Locate and identify every blood parasite.
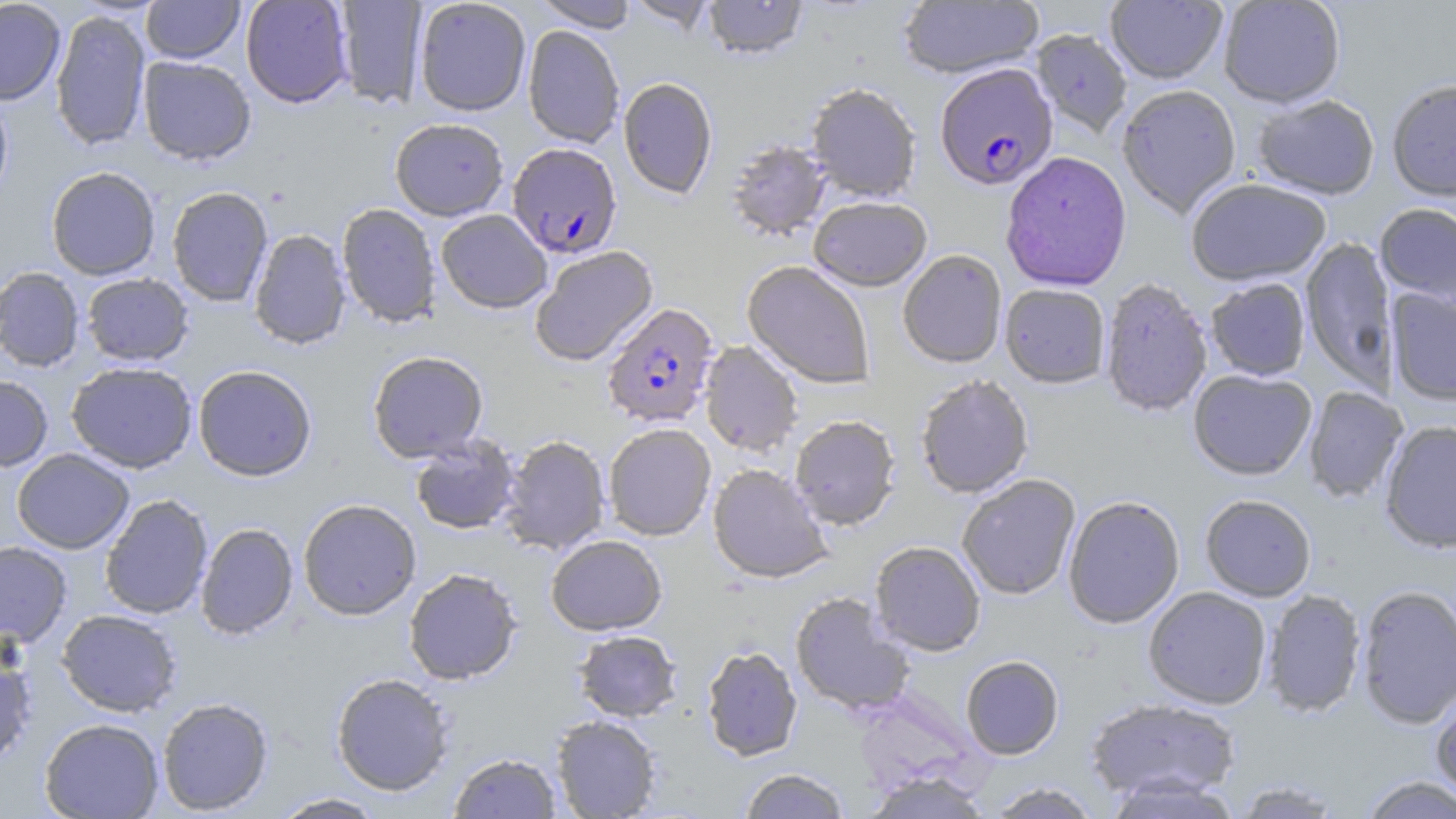

Approximate bounding boxes as named x1/y1/x2/y2 corners in pixels.
Plasmodium falciparum-infected red blood cells: (x1=934, y1=63, x2=1057, y2=190), (x1=507, y1=142, x2=622, y2=258), (x1=602, y1=303, x2=719, y2=429).
No Plasmodium ovale, Plasmodium malariae, Plasmodium vivax, Babesia divergens, or Trypanosoma brucei observed.

Summary:
  - Uninfected red blood cell locations: (x1=0, y1=0, x2=66, y2=105), (x1=141, y1=0, x2=244, y2=64), (x1=240, y1=0, x2=354, y2=108), (x1=413, y1=0, x2=531, y2=116), (x1=533, y1=0, x2=639, y2=32), (x1=624, y1=0, x2=718, y2=33), (x1=703, y1=0, x2=807, y2=60), (x1=1106, y1=0, x2=1226, y2=85), (x1=1218, y1=0, x2=1345, y2=108), (x1=333, y1=1, x2=428, y2=108), (x1=898, y1=1, x2=1044, y2=79), (x1=50, y1=9, x2=151, y2=151), (x1=522, y1=25, x2=624, y2=147), (x1=1031, y1=30, x2=1132, y2=137), (x1=138, y1=56, x2=256, y2=165), (x1=618, y1=77, x2=718, y2=199), (x1=1386, y1=80, x2=1456, y2=202), (x1=805, y1=83, x2=922, y2=203), (x1=1117, y1=84, x2=1242, y2=218), (x1=0, y1=91, x2=13, y2=209), (x1=1252, y1=94, x2=1380, y2=200), (x1=390, y1=118, x2=509, y2=221), (x1=725, y1=138, x2=832, y2=242), (x1=1000, y1=152, x2=1132, y2=292), (x1=46, y1=166, x2=161, y2=280), (x1=1186, y1=178, x2=1331, y2=287), (x1=167, y1=186, x2=273, y2=306), (x1=808, y1=196, x2=932, y2=291), (x1=1375, y1=202, x2=1456, y2=308), (x1=337, y1=203, x2=441, y2=328), (x1=436, y1=209, x2=552, y2=313), (x1=249, y1=229, x2=351, y2=350), (x1=1300, y1=236, x2=1398, y2=390), (x1=529, y1=245, x2=658, y2=367), (x1=897, y1=250, x2=1007, y2=368), (x1=742, y1=260, x2=875, y2=389), (x1=0, y1=266, x2=85, y2=372), (x1=81, y1=273, x2=194, y2=366), (x1=1205, y1=278, x2=1311, y2=381), (x1=1099, y1=279, x2=1212, y2=417), (x1=999, y1=283, x2=1110, y2=388), (x1=1386, y1=287, x2=1456, y2=406), (x1=699, y1=340, x2=804, y2=457), (x1=368, y1=350, x2=488, y2=463), (x1=66, y1=361, x2=197, y2=473), (x1=192, y1=365, x2=317, y2=481), (x1=1188, y1=369, x2=1317, y2=480), (x1=915, y1=375, x2=1034, y2=498), (x1=0, y1=376, x2=53, y2=471), (x1=1304, y1=386, x2=1407, y2=504), (x1=790, y1=414, x2=901, y2=529), (x1=1380, y1=421, x2=1456, y2=553), (x1=603, y1=423, x2=716, y2=541), (x1=499, y1=434, x2=610, y2=555), (x1=409, y1=435, x2=521, y2=535), (x1=12, y1=449, x2=134, y2=554), (x1=708, y1=463, x2=832, y2=584), (x1=956, y1=474, x2=1081, y2=600), (x1=99, y1=494, x2=213, y2=619), (x1=1200, y1=494, x2=1317, y2=602), (x1=1063, y1=496, x2=1185, y2=628), (x1=297, y1=498, x2=421, y2=620), (x1=196, y1=522, x2=298, y2=639), (x1=546, y1=534, x2=667, y2=635), (x1=0, y1=541, x2=72, y2=646), (x1=869, y1=541, x2=986, y2=656), (x1=403, y1=567, x2=523, y2=685), (x1=1356, y1=584, x2=1456, y2=729), (x1=1143, y1=587, x2=1272, y2=709), (x1=1261, y1=589, x2=1367, y2=718), (x1=790, y1=591, x2=916, y2=717), (x1=56, y1=609, x2=182, y2=716), (x1=573, y1=630, x2=682, y2=722), (x1=0, y1=637, x2=38, y2=768), (x1=701, y1=646, x2=802, y2=760), (x1=960, y1=655, x2=1064, y2=760), (x1=331, y1=672, x2=454, y2=795), (x1=1431, y1=689, x2=1456, y2=804), (x1=157, y1=697, x2=273, y2=815), (x1=1085, y1=697, x2=1241, y2=803), (x1=551, y1=715, x2=661, y2=818), (x1=39, y1=718, x2=164, y2=818), (x1=449, y1=752, x2=562, y2=818), (x1=738, y1=768, x2=850, y2=818), (x1=863, y1=772, x2=991, y2=818), (x1=1102, y1=774, x2=1243, y2=819), (x1=1358, y1=775, x2=1456, y2=818), (x1=1229, y1=780, x2=1349, y2=818), (x1=984, y1=782, x2=1102, y2=818), (x1=269, y1=792, x2=387, y2=818)
  - Slide-level diagnosis: Plasmodium falciparum
  - Magnification: 1000x
  - Field of view: single
  - Modality: optical microscopy
  - Stain: May-Grünwald-Giemsa
  - Image size: 1456×819 pixels
  - Preparation: thin blood smear